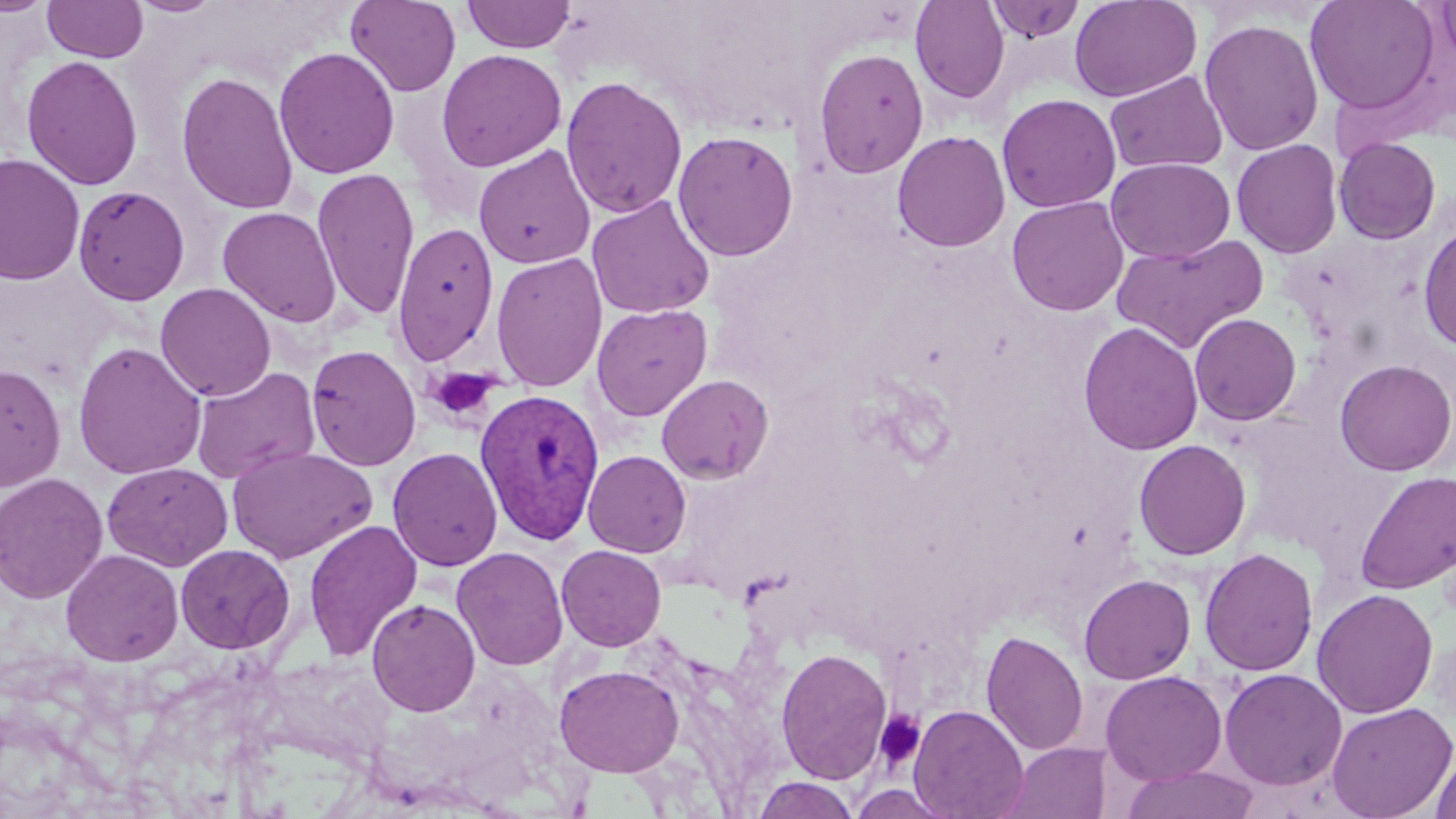

slide-level diagnosis = Plasmodium vivax
field of view = single
platelet locations = approximate bounding boxes as (x1,y1)-(x2,y2) corner pairs in pixels: (427,367)-(502,424), (874,709)-(925,769)
stain = May-Grünwald-Giemsa
modality = light microscopy
uninfected red blood cell locations = approximate bounding boxes as (x1,y1)-(x2,y2) corner pairs in pixels: (0,0)-(54,17), (130,0)-(222,17), (461,0)-(577,53), (910,0)-(1010,103), (1069,0)-(1202,102), (1304,0)-(1440,115), (1434,0)-(1456,71), (42,1)-(149,63), (345,1)-(461,97), (984,1)-(1086,42), (1199,17)-(1324,156), (274,47)-(399,179), (813,48)-(929,179), (436,49)-(567,172), (21,54)-(143,190), (176,70)-(299,215), (1105,70)-(1228,174), (560,76)-(688,219), (997,93)-(1121,213), (672,130)-(799,262), (892,130)-(1011,252), (1333,137)-(1441,244), (1231,139)-(1343,258), (474,144)-(595,269), (0,153)-(85,286), (1106,157)-(1236,263), (312,166)-(420,322), (73,184)-(190,306), (587,195)-(716,320), (1006,196)-(1129,317), (217,206)-(342,327), (1417,220)-(1456,353), (391,221)-(499,366), (1112,233)-(1270,352), (491,252)-(608,392), (155,282)-(277,401), (591,303)-(713,421), (1189,313)-(1302,425), (1079,321)-(1203,456), (73,341)-(207,481), (306,344)-(422,472), (1334,359)-(1456,476), (0,363)-(66,492), (191,366)-(321,484), (657,374)-(774,485), (1134,439)-(1252,560), (226,445)-(377,564), (387,447)-(503,572), (583,450)-(691,557), (102,461)-(233,571), (1354,470)-(1456,594), (0,473)-(110,604), (304,518)-(423,662), (175,544)-(295,654), (556,544)-(667,651), (451,546)-(569,670), (1199,547)-(1319,677), (60,549)-(184,666), (1079,573)-(1196,685), (1312,589)-(1439,719), (367,598)-(481,717), (981,629)-(1088,756), (775,648)-(893,784), (553,664)-(684,777), (1219,668)-(1347,790), (1100,670)-(1227,785), (1326,701)-(1456,819), (908,703)-(1029,819), (1001,742)-(1111,819), (1431,746)-(1456,819), (1120,764)-(1262,819), (751,775)-(860,818)
preparation = thin blood film
magnification = 1000x
image size = 1456×819 pixels
Plasmodium vivax-infected red blood cell locations = approximate bounding boxes as (x1,y1)-(x2,y2) corner pairs in pixels: (474,388)-(604,545)